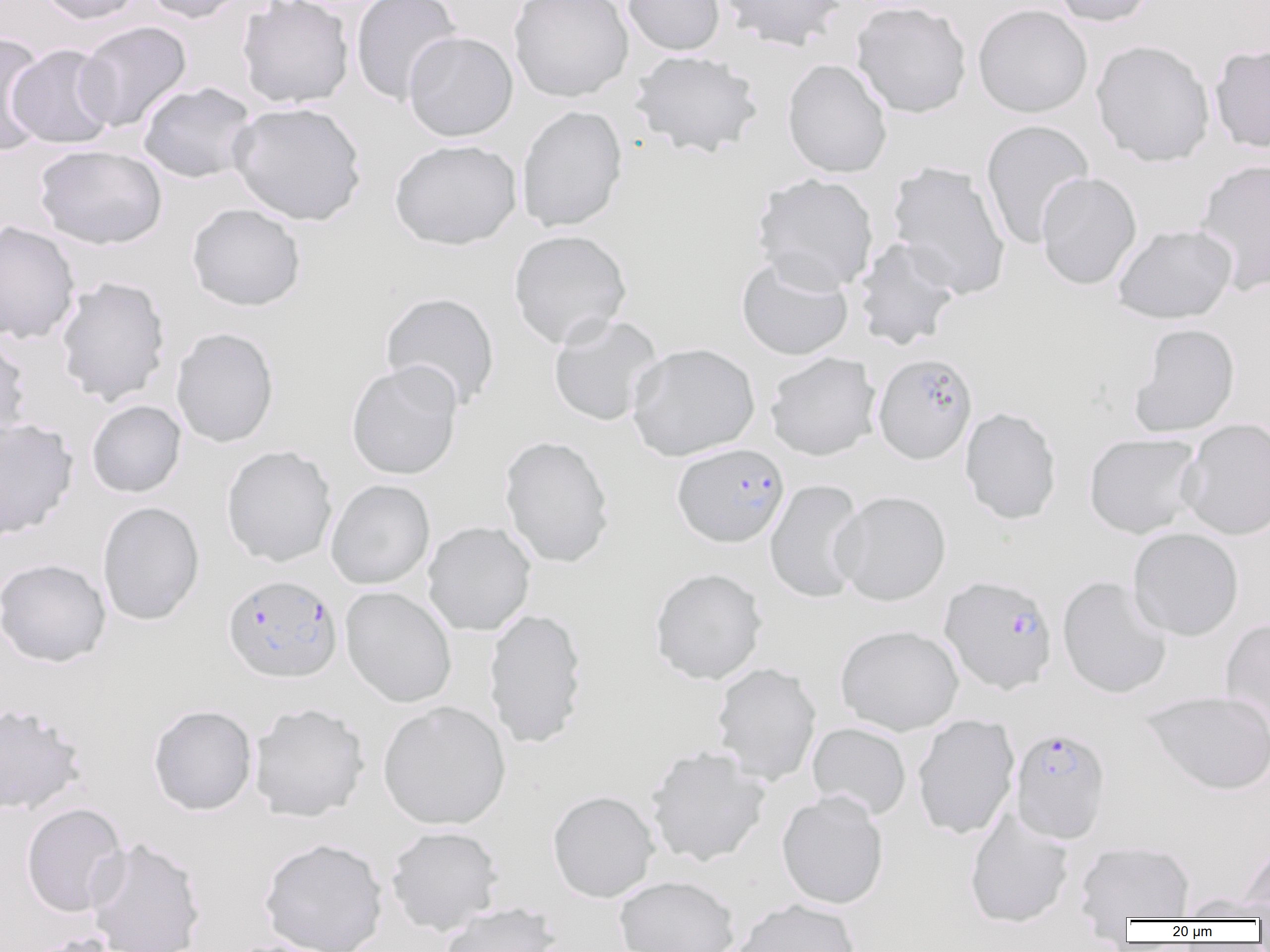
Summary:
  - Coordinate format: approximate bounding boxes as named x1/y1/x2/y2 corners in pixels
  - Plasmodium falciparum-infected red blood cell locations: (x1=872, y1=352, x2=978, y2=465), (x1=673, y1=443, x2=790, y2=548), (x1=223, y1=574, x2=342, y2=683), (x1=938, y1=574, x2=1058, y2=695), (x1=1010, y1=726, x2=1111, y2=843)
  - Uninfected red blood cell locations: (x1=34, y1=0, x2=144, y2=25), (x1=141, y1=0, x2=251, y2=24), (x1=237, y1=0, x2=354, y2=109), (x1=350, y1=0, x2=462, y2=106), (x1=508, y1=0, x2=633, y2=102), (x1=623, y1=0, x2=725, y2=56), (x1=718, y1=0, x2=846, y2=50), (x1=1049, y1=0, x2=1157, y2=27), (x1=851, y1=1, x2=972, y2=118), (x1=973, y1=4, x2=1093, y2=118), (x1=75, y1=21, x2=192, y2=133), (x1=403, y1=31, x2=518, y2=142), (x1=0, y1=33, x2=50, y2=156), (x1=1091, y1=40, x2=1216, y2=167), (x1=7, y1=43, x2=118, y2=149), (x1=1209, y1=43, x2=1270, y2=153), (x1=629, y1=50, x2=764, y2=159), (x1=782, y1=58, x2=893, y2=178), (x1=137, y1=81, x2=257, y2=184), (x1=229, y1=100, x2=366, y2=226), (x1=516, y1=105, x2=627, y2=232), (x1=980, y1=119, x2=1094, y2=250), (x1=389, y1=139, x2=522, y2=250), (x1=34, y1=144, x2=167, y2=250), (x1=1193, y1=158, x2=1270, y2=296), (x1=887, y1=161, x2=1012, y2=299), (x1=1035, y1=172, x2=1141, y2=290), (x1=752, y1=173, x2=879, y2=293), (x1=186, y1=203, x2=306, y2=311), (x1=0, y1=220, x2=80, y2=344), (x1=1112, y1=223, x2=1237, y2=324), (x1=508, y1=229, x2=632, y2=348), (x1=852, y1=237, x2=962, y2=350), (x1=736, y1=254, x2=854, y2=361), (x1=55, y1=276, x2=171, y2=406), (x1=380, y1=291, x2=501, y2=413), (x1=547, y1=313, x2=664, y2=427), (x1=1129, y1=322, x2=1240, y2=438), (x1=171, y1=327, x2=279, y2=448), (x1=0, y1=333, x2=31, y2=452), (x1=626, y1=342, x2=760, y2=461), (x1=765, y1=352, x2=881, y2=461), (x1=346, y1=361, x2=463, y2=480), (x1=86, y1=399, x2=187, y2=498), (x1=960, y1=407, x2=1062, y2=525), (x1=1179, y1=417, x2=1270, y2=540), (x1=0, y1=418, x2=78, y2=540), (x1=1083, y1=433, x2=1203, y2=539), (x1=499, y1=435, x2=615, y2=568), (x1=221, y1=445, x2=338, y2=567), (x1=765, y1=478, x2=867, y2=604), (x1=326, y1=479, x2=435, y2=589), (x1=832, y1=490, x2=951, y2=606), (x1=97, y1=501, x2=205, y2=625), (x1=422, y1=521, x2=536, y2=636), (x1=1128, y1=528, x2=1244, y2=641), (x1=0, y1=558, x2=111, y2=667), (x1=649, y1=567, x2=768, y2=685), (x1=1057, y1=576, x2=1172, y2=699), (x1=340, y1=586, x2=457, y2=708), (x1=483, y1=607, x2=588, y2=749), (x1=1220, y1=617, x2=1270, y2=732), (x1=835, y1=624, x2=963, y2=735), (x1=711, y1=662, x2=822, y2=786), (x1=1141, y1=689, x2=1270, y2=796), (x1=378, y1=701, x2=511, y2=830), (x1=1, y1=702, x2=87, y2=815), (x1=249, y1=702, x2=370, y2=822), (x1=148, y1=705, x2=258, y2=816), (x1=912, y1=713, x2=1019, y2=839), (x1=807, y1=722, x2=911, y2=820), (x1=645, y1=744, x2=771, y2=867), (x1=548, y1=790, x2=660, y2=902), (x1=777, y1=790, x2=889, y2=909), (x1=21, y1=802, x2=129, y2=917), (x1=965, y1=808, x2=1075, y2=929), (x1=385, y1=825, x2=504, y2=936), (x1=85, y1=836, x2=206, y2=952), (x1=258, y1=837, x2=388, y2=952), (x1=1238, y1=839, x2=1270, y2=920), (x1=1074, y1=840, x2=1195, y2=921), (x1=614, y1=875, x2=740, y2=952), (x1=1179, y1=893, x2=1270, y2=922), (x1=729, y1=898, x2=862, y2=952), (x1=439, y1=902, x2=562, y2=952), (x1=20, y1=932, x2=128, y2=952), (x1=220, y1=938, x2=337, y2=952)
  - Slide-level diagnosis: Plasmodium falciparum
  - Image size: 1270×952 pixels
  - Magnification: 1000x
  - Preparation: thin blood smear
  - Modality: light microscopy
  - Field of view: one of a larger specimen